Classify this cell by malaria status.
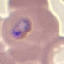

Parasitized.

capture = smartphone through the microscope eyepiece
image type = cell patch, automatically extracted from a larger field of view and resized to 64 × 64 pixels
stain = Giemsa
preparation = thin blood smear